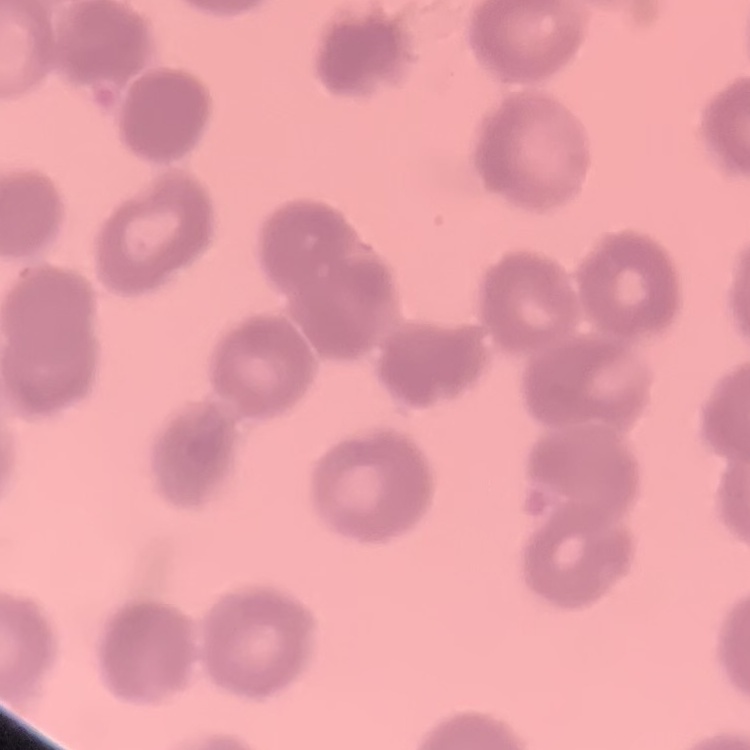

Summary:
  - Erythrocyte morphology: rouleaux formation
  - Image type: one tile cut from a larger photomicrograph
  - Preparation: thin blood smear
  - Stain: Field's or Giemsa